Evaluate for malaria.
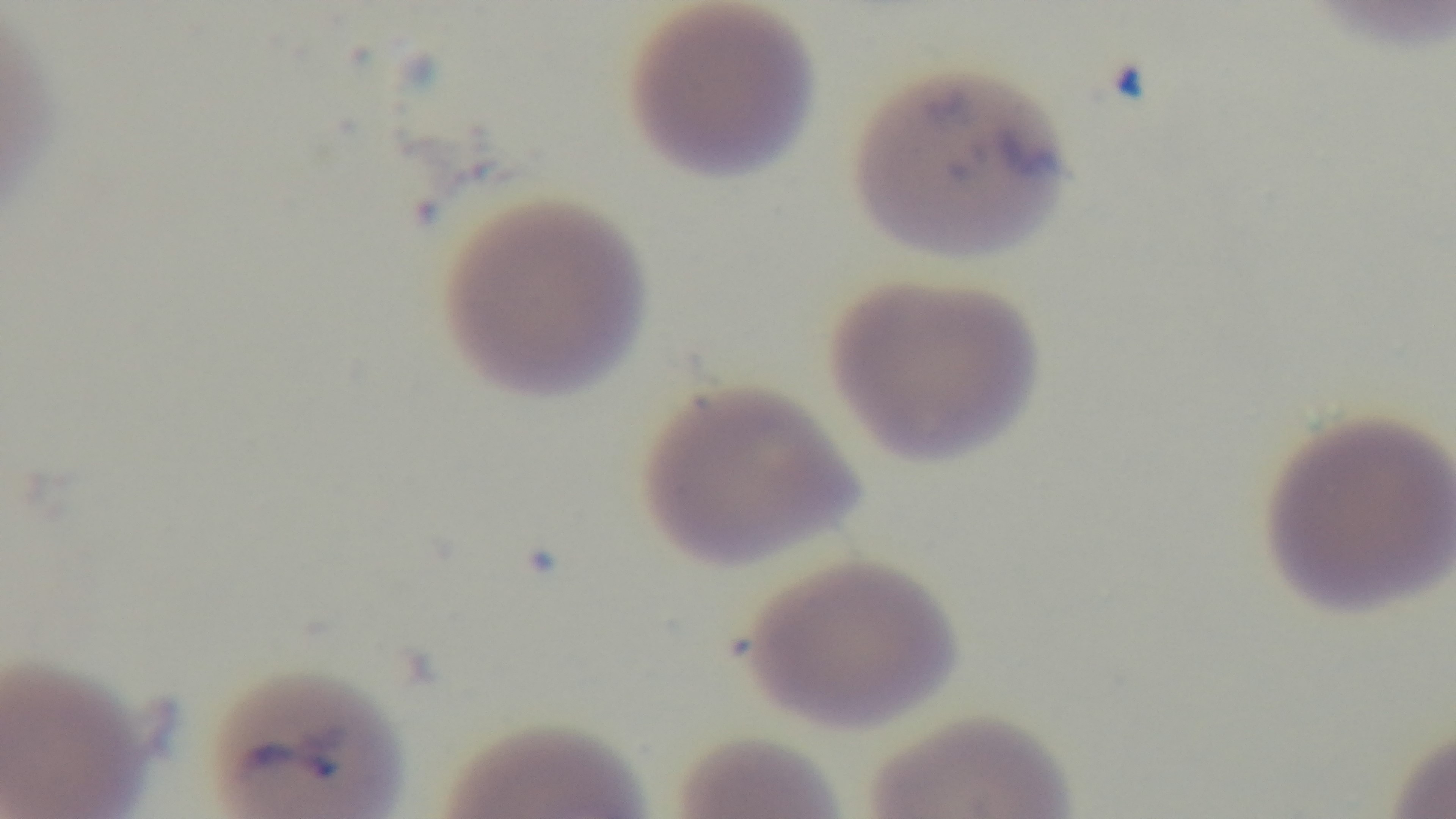
Infected.

Giemsa-stained. Mounted 4K digital camera. 100x oil-immersion objective. Photomicrograph. Single field of view. Preparation: thin.